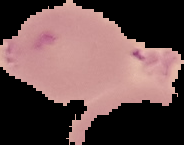

malaria_status: uninfected
preparation: thin blood film
image_type: segmented cell region with the area outside set to black
image_size: 184×145 pixels